Point out each malaria parasite and each leukocyte.
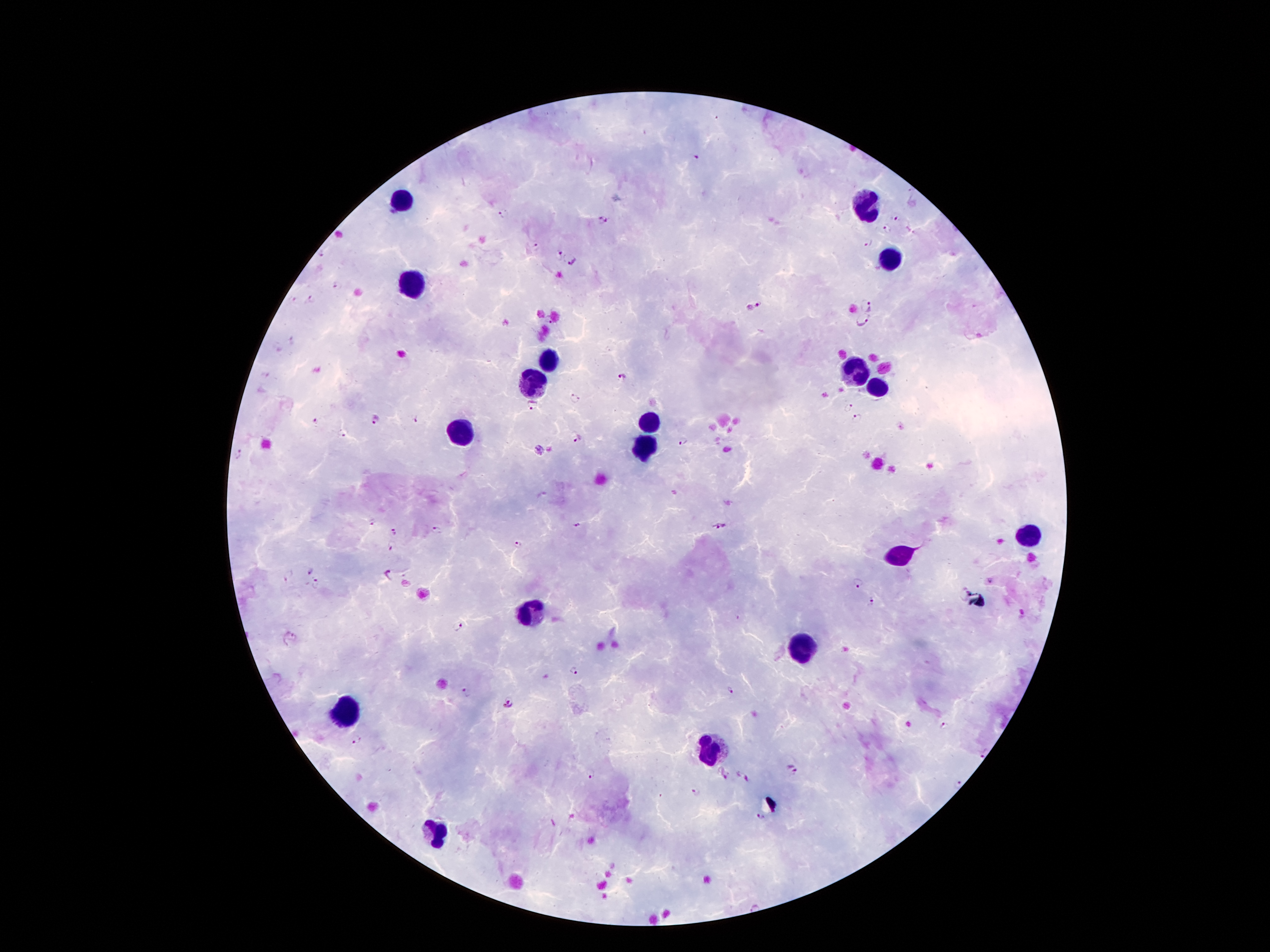

Approximate centers as [x, y] in pixels.
Malaria parasites: [694, 156], [502, 214], [895, 219], [604, 220], [887, 228], [866, 241], [536, 247], [560, 253], [320, 255], [574, 261], [335, 285], [290, 297], [310, 298], [866, 303], [755, 306], [863, 319], [292, 342], [622, 376], [574, 397], [530, 405], [850, 406], [416, 418], [857, 418], [314, 421], [376, 421], [343, 435], [575, 436], [685, 442], [539, 451], [236, 454], [373, 523], [577, 525], [718, 525], [436, 528], [394, 532], [518, 544], [392, 547], [308, 571], [289, 574], [387, 576], [317, 585], [856, 585], [874, 601], [458, 627], [293, 638], [575, 669], [727, 691], [466, 692], [508, 702], [944, 726], [356, 739], [982, 750], [791, 768], [592, 774], [722, 774], [743, 776], [956, 784], [696, 794], [760, 818].
Leukocytes: [404, 200], [865, 203], [892, 258], [411, 286], [548, 358], [853, 371], [530, 376], [873, 386], [648, 425], [466, 434], [643, 447], [1029, 536], [900, 555], [529, 610], [800, 647], [345, 714], [711, 749], [435, 835].

Single field of view. 100x magnification. Thick blood smear. Image is 1270×952 pixels. Giemsa-stained preparation. Patient malaria status: infected with Plasmodium falciparum. Photographed through the microscope eyepiece with a smartphone camera.